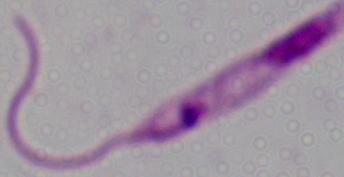
Summary:
  - Modality: photomicrograph
  - Magnification: 1000x
  - Identification: Leishmania